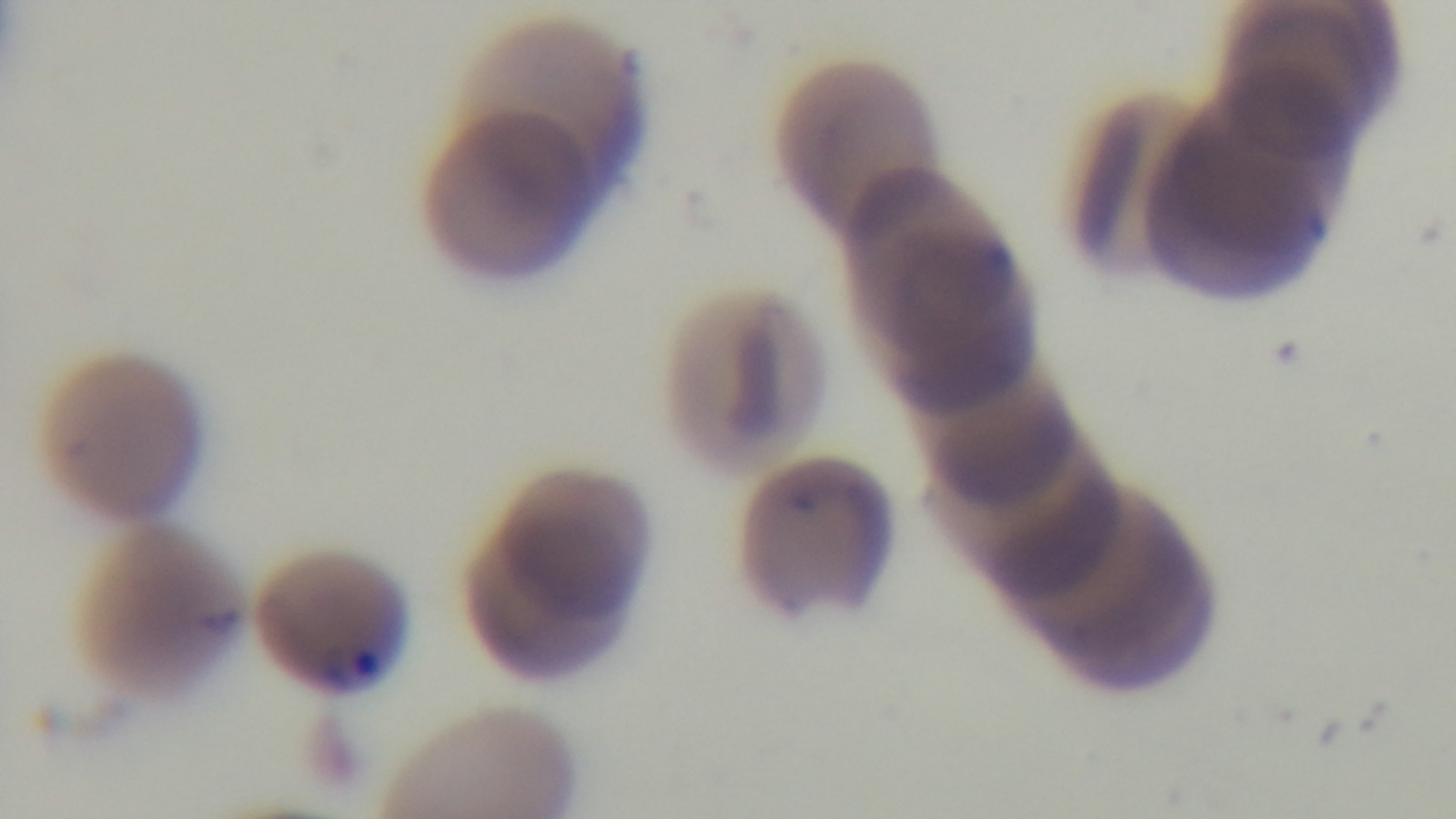
{
  "objective": "100x oil immersion",
  "capture": "mounted 4K digital camera",
  "malaria_status": "positive",
  "field_of_view": "one from the slide",
  "stain": "Giemsa",
  "modality": "light microscopy",
  "preparation": "thin blood film"
}